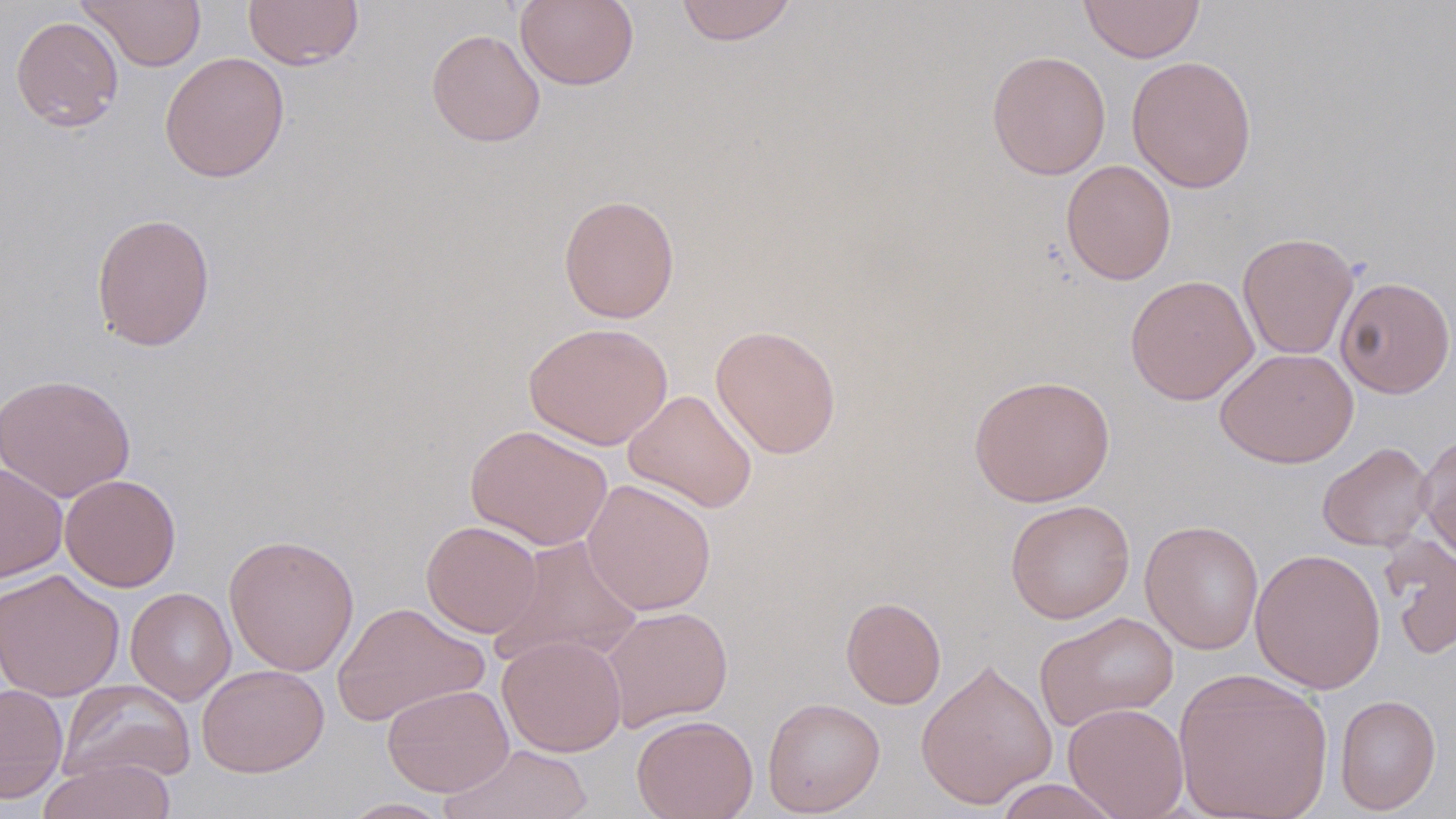

Approximate bounding boxes as named x1/y1/x2/y2 corners in pixels. Uninfected red blood cell locations: (x1=77, y1=0, x2=207, y2=71), (x1=243, y1=0, x2=364, y2=70), (x1=514, y1=0, x2=639, y2=91), (x1=674, y1=0, x2=798, y2=46), (x1=1079, y1=0, x2=1205, y2=62), (x1=10, y1=15, x2=124, y2=132), (x1=426, y1=28, x2=545, y2=147), (x1=986, y1=50, x2=1111, y2=179), (x1=159, y1=52, x2=290, y2=182), (x1=1126, y1=55, x2=1257, y2=193), (x1=1061, y1=159, x2=1177, y2=285), (x1=558, y1=194, x2=680, y2=323), (x1=90, y1=212, x2=216, y2=352), (x1=1237, y1=231, x2=1359, y2=359), (x1=1125, y1=274, x2=1258, y2=405), (x1=1335, y1=276, x2=1456, y2=398), (x1=523, y1=322, x2=673, y2=450), (x1=711, y1=324, x2=842, y2=459), (x1=1215, y1=348, x2=1358, y2=468), (x1=0, y1=373, x2=136, y2=502), (x1=968, y1=373, x2=1115, y2=507), (x1=622, y1=389, x2=758, y2=513), (x1=465, y1=424, x2=612, y2=550), (x1=1416, y1=431, x2=1456, y2=563), (x1=1317, y1=441, x2=1434, y2=552), (x1=0, y1=462, x2=68, y2=583), (x1=60, y1=474, x2=181, y2=591), (x1=582, y1=478, x2=717, y2=616), (x1=1005, y1=499, x2=1135, y2=623), (x1=421, y1=520, x2=542, y2=637), (x1=1139, y1=520, x2=1264, y2=654), (x1=1379, y1=533, x2=1456, y2=660), (x1=223, y1=534, x2=360, y2=677), (x1=491, y1=535, x2=645, y2=667), (x1=1250, y1=548, x2=1386, y2=694), (x1=0, y1=568, x2=125, y2=702), (x1=125, y1=587, x2=237, y2=705), (x1=840, y1=596, x2=947, y2=709), (x1=331, y1=601, x2=489, y2=727), (x1=601, y1=605, x2=733, y2=731), (x1=1034, y1=611, x2=1179, y2=732), (x1=497, y1=635, x2=627, y2=757), (x1=915, y1=658, x2=1058, y2=809), (x1=196, y1=663, x2=330, y2=777), (x1=1173, y1=668, x2=1334, y2=819), (x1=58, y1=679, x2=196, y2=785), (x1=0, y1=683, x2=68, y2=803), (x1=382, y1=683, x2=514, y2=797), (x1=1334, y1=694, x2=1441, y2=815), (x1=762, y1=696, x2=885, y2=816), (x1=1063, y1=702, x2=1189, y2=819), (x1=632, y1=713, x2=758, y2=819), (x1=440, y1=744, x2=594, y2=819), (x1=37, y1=756, x2=176, y2=819), (x1=991, y1=778, x2=1127, y2=819), (x1=335, y1=798, x2=455, y2=818). Slide-level diagnosis: no evidence of blood parasites. Single field of view. Image is 1456×819 pixels. Thin blood film. Light microscopy. May-Grünwald-Giemsa stain. Captured at 1000x magnification.